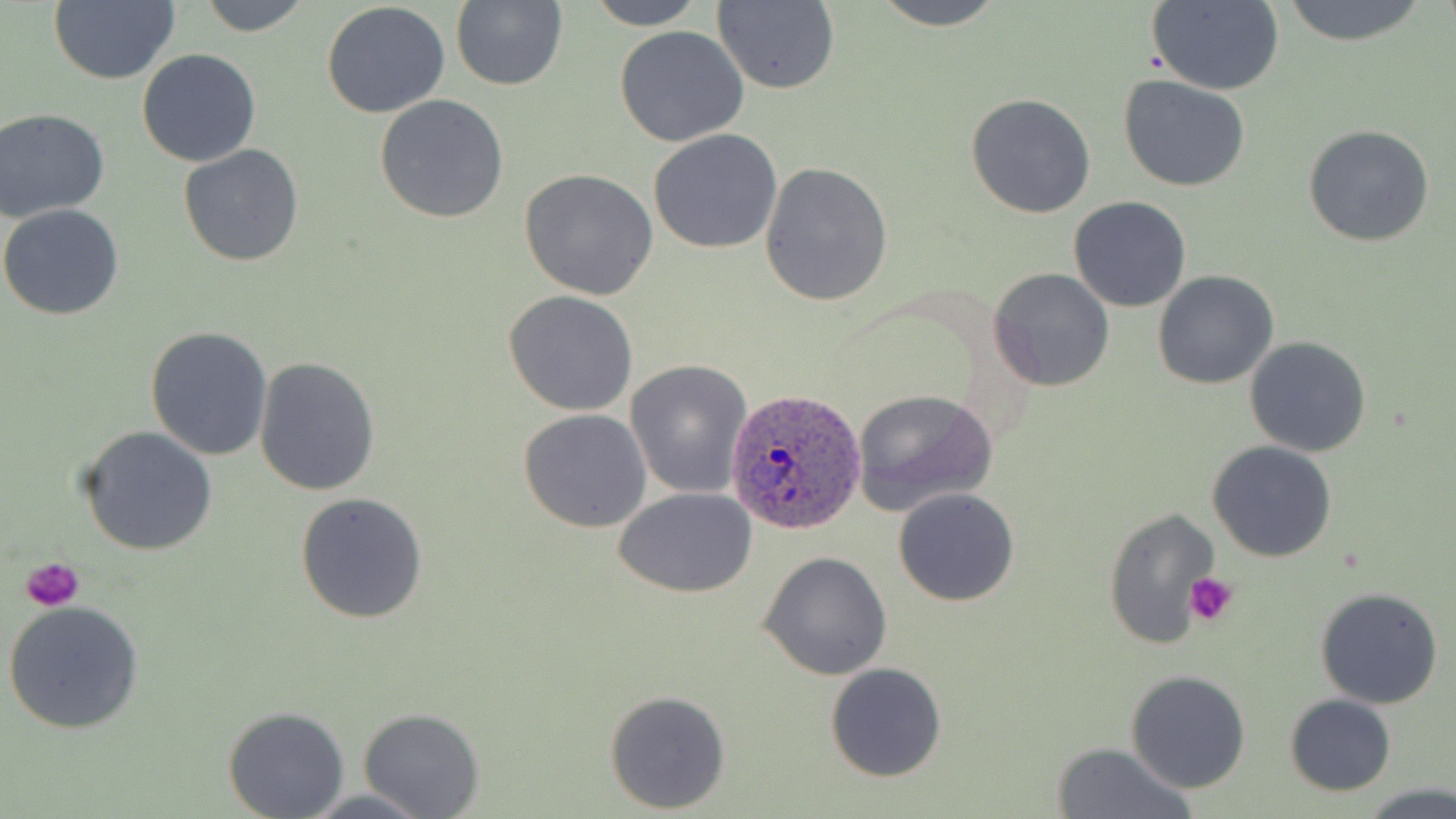 Approximate bounding boxes as [x1, y1, x2, y2] in pixels. Plasmodium ovale-infected red blood cell locations: [726, 387, 868, 535]. Uninfected red blood cell locations: [49, 0, 181, 85], [195, 0, 315, 36], [589, 0, 707, 29], [869, 0, 1010, 29], [1279, 0, 1431, 46], [450, 1, 568, 91], [710, 1, 840, 93], [1145, 1, 1285, 94], [320, 2, 451, 119], [614, 26, 749, 148], [136, 48, 262, 167], [1120, 75, 1250, 191], [374, 94, 509, 225], [966, 94, 1096, 218], [1, 106, 112, 224], [1303, 124, 1436, 247], [648, 129, 782, 253], [177, 144, 305, 267], [759, 163, 893, 306], [519, 167, 661, 301], [1068, 197, 1192, 313], [0, 203, 125, 320], [987, 267, 1114, 392], [1153, 270, 1278, 389], [503, 290, 638, 415], [145, 327, 274, 463], [1233, 333, 1358, 566], [1244, 336, 1372, 457], [254, 355, 382, 496], [625, 359, 752, 499], [851, 388, 998, 513], [518, 409, 652, 533], [77, 426, 220, 556], [1207, 441, 1337, 563], [614, 486, 758, 599], [893, 487, 1020, 606], [295, 491, 429, 625], [1101, 505, 1218, 652], [759, 551, 891, 680], [1314, 587, 1444, 709], [4, 600, 145, 734], [825, 663, 947, 782], [1125, 670, 1252, 794], [605, 689, 731, 811], [1284, 694, 1396, 795], [222, 706, 350, 818], [358, 708, 484, 818], [1051, 741, 1197, 819], [1365, 784, 1456, 818], [297, 789, 434, 818]. Platelet locations: [22, 557, 84, 613], [1186, 572, 1240, 627]. Slide-level diagnosis: Plasmodium ovale. 1000x magnification. Optical microscopy. Thin blood film. May-Grünwald-Giemsa-stained preparation. Image is 1456×819 pixels. Single field of view.